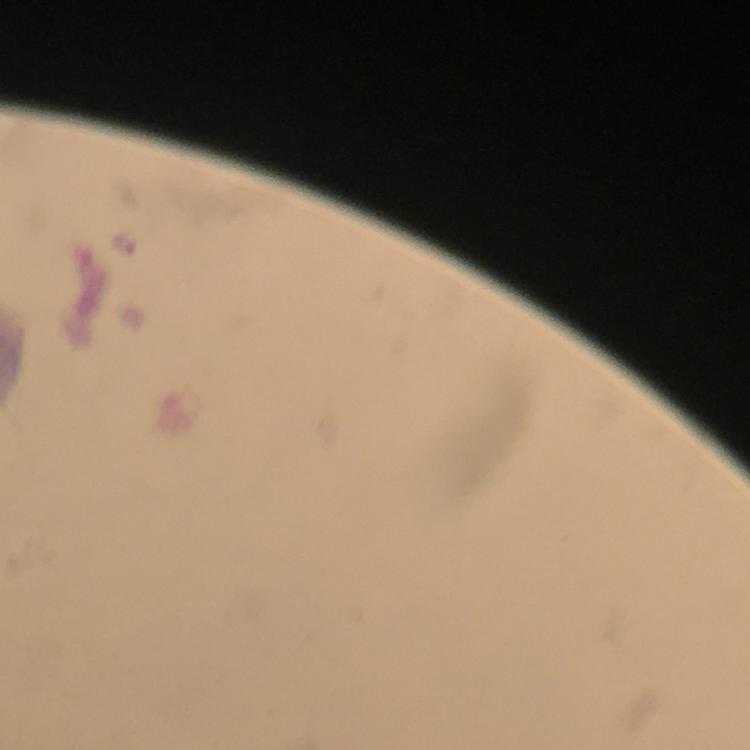

Approximate centers as [x, y] in pixels.
Summary:
  - Plasmodium parasite locations: [127, 244]
  - Preparation: thick blood smear
  - Cropped from: a single field of view
  - Stain: Giemsa
  - Image size: 750×750 pixels
  - Context: from a diagnostic examination for malaria
  - Capture: smartphone photograph through a microscope
  - Magnification: 100x
  - Immersion oil: used